Describe the morphology of the erythrocytes.
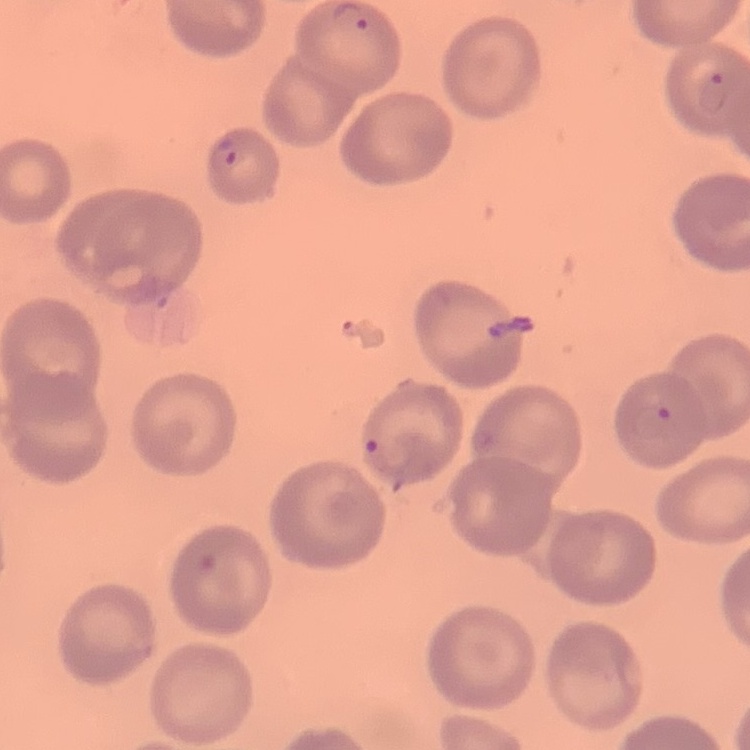
They show no rouleaux formation.

Summary:
  - Preparation: thin peripheral smear
  - Image type: one tile cut from a larger photomicrograph
  - Stain: Field's or Giemsa